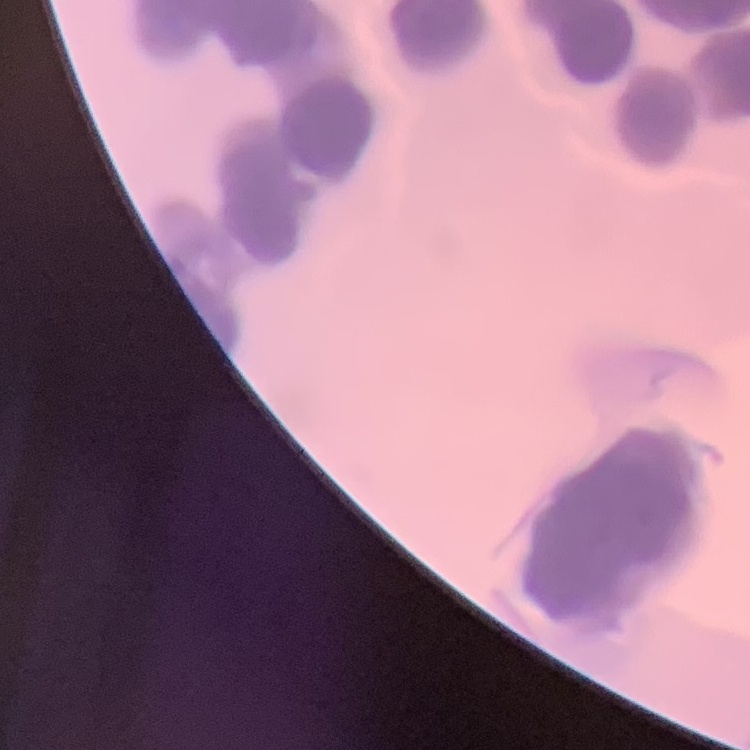

red blood cell morphology = rouleaux formation
image type = one tile cut from a larger photomicrograph
stain = Field's or Giemsa
preparation = thin peripheral smear